Give the extent of all uninfected red blood cells.
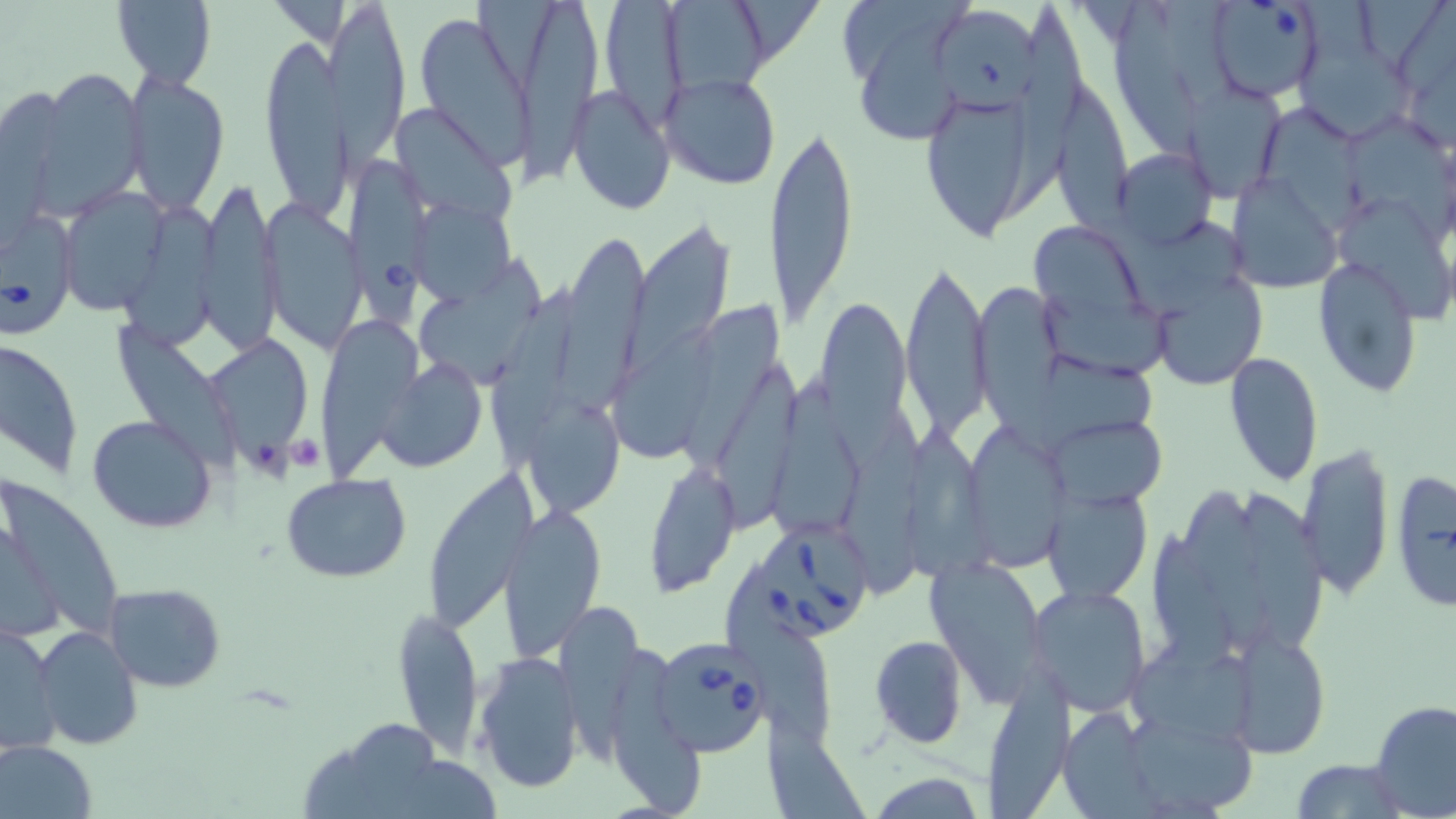

Approximate bounding boxes as named x1/y1/x2/y2 corners in pixels.
Uninfected red blood cells: (x1=334, y1=0, x2=407, y2=170), (x1=110, y1=1, x2=217, y2=87), (x1=268, y1=1, x2=339, y2=46), (x1=598, y1=1, x2=689, y2=132), (x1=671, y1=1, x2=771, y2=98), (x1=1003, y1=1, x2=1077, y2=220), (x1=845, y1=2, x2=973, y2=84), (x1=1111, y1=2, x2=1200, y2=159), (x1=508, y1=3, x2=599, y2=187), (x1=415, y1=13, x2=534, y2=167), (x1=942, y1=14, x2=1042, y2=117), (x1=261, y1=32, x2=345, y2=228), (x1=856, y1=37, x2=973, y2=137), (x1=1298, y1=47, x2=1414, y2=141), (x1=34, y1=65, x2=147, y2=214), (x1=123, y1=68, x2=230, y2=213), (x1=660, y1=73, x2=782, y2=191), (x1=570, y1=83, x2=676, y2=218), (x1=1181, y1=85, x2=1285, y2=200), (x1=919, y1=87, x2=1047, y2=242), (x1=1055, y1=88, x2=1135, y2=235), (x1=395, y1=111, x2=515, y2=222), (x1=1262, y1=111, x2=1365, y2=241), (x1=1346, y1=117, x2=1456, y2=252), (x1=765, y1=122, x2=860, y2=331), (x1=1114, y1=147, x2=1217, y2=253), (x1=1227, y1=172, x2=1344, y2=292), (x1=197, y1=179, x2=280, y2=354), (x1=59, y1=187, x2=172, y2=315), (x1=263, y1=201, x2=364, y2=354), (x1=418, y1=202, x2=512, y2=304), (x1=126, y1=207, x2=229, y2=361), (x1=1342, y1=209, x2=1454, y2=325), (x1=1029, y1=218, x2=1150, y2=325), (x1=1115, y1=221, x2=1244, y2=320), (x1=631, y1=224, x2=733, y2=352), (x1=556, y1=236, x2=647, y2=417), (x1=901, y1=254, x2=994, y2=443), (x1=1314, y1=256, x2=1425, y2=398), (x1=417, y1=258, x2=542, y2=386), (x1=1154, y1=259, x2=1268, y2=390), (x1=493, y1=278, x2=580, y2=476), (x1=972, y1=280, x2=1061, y2=417), (x1=1046, y1=293, x2=1168, y2=381), (x1=813, y1=296, x2=914, y2=439), (x1=685, y1=308, x2=784, y2=473), (x1=320, y1=322, x2=423, y2=484), (x1=115, y1=328, x2=243, y2=476), (x1=612, y1=329, x2=728, y2=460), (x1=1, y1=336, x2=83, y2=478), (x1=213, y1=338, x2=305, y2=483), (x1=1224, y1=352, x2=1324, y2=488), (x1=1034, y1=359, x2=1166, y2=449), (x1=379, y1=360, x2=486, y2=471), (x1=713, y1=360, x2=804, y2=529), (x1=768, y1=374, x2=854, y2=554), (x1=530, y1=406, x2=617, y2=518), (x1=87, y1=413, x2=218, y2=532), (x1=1057, y1=414, x2=1167, y2=510), (x1=846, y1=421, x2=924, y2=596), (x1=966, y1=422, x2=1073, y2=572), (x1=905, y1=423, x2=987, y2=580), (x1=1298, y1=439, x2=1396, y2=603), (x1=644, y1=458, x2=738, y2=596), (x1=422, y1=467, x2=536, y2=633), (x1=1390, y1=469, x2=1456, y2=615), (x1=282, y1=473, x2=413, y2=584), (x1=2, y1=475, x2=119, y2=639), (x1=1044, y1=486, x2=1152, y2=603), (x1=1184, y1=488, x2=1277, y2=661), (x1=1240, y1=492, x2=1329, y2=651), (x1=498, y1=504, x2=606, y2=657), (x1=1, y1=511, x2=62, y2=645), (x1=1150, y1=537, x2=1243, y2=675), (x1=925, y1=558, x2=1046, y2=712), (x1=104, y1=583, x2=228, y2=693), (x1=1029, y1=584, x2=1153, y2=717), (x1=726, y1=599, x2=837, y2=749), (x1=556, y1=602, x2=643, y2=772), (x1=393, y1=608, x2=485, y2=757), (x1=1, y1=618, x2=61, y2=758), (x1=32, y1=624, x2=142, y2=750), (x1=1226, y1=627, x2=1331, y2=758), (x1=869, y1=635, x2=968, y2=748), (x1=1126, y1=641, x2=1268, y2=754), (x1=615, y1=646, x2=708, y2=818), (x1=475, y1=653, x2=586, y2=795), (x1=986, y1=668, x2=1076, y2=819), (x1=1369, y1=700, x2=1456, y2=818), (x1=1060, y1=708, x2=1160, y2=815), (x1=764, y1=713, x2=865, y2=819), (x1=347, y1=721, x2=437, y2=819), (x1=1133, y1=721, x2=1254, y2=818), (x1=1, y1=740, x2=98, y2=819), (x1=1291, y1=758, x2=1410, y2=819), (x1=869, y1=772, x2=986, y2=818).

slide-level diagnosis = Babesia divergens
stain = May-Grünwald-Giemsa
image size = 1456×819 pixels
Babesia divergens-infected red blood cell locations = approximate bounding boxes as named x1/y1/x2/y2 corners in pixels: (x1=1205, y1=1, x2=1326, y2=102), (x1=346, y1=155, x2=427, y2=327), (x1=0, y1=209, x2=79, y2=337), (x1=759, y1=526, x2=868, y2=644), (x1=658, y1=642, x2=765, y2=758)
field of view = one of a larger specimen
preparation = thin blood film
magnification = 1000x
modality = light microscopy
platelet locations = approximate bounding boxes as named x1/y1/x2/y2 corners in pixels: (x1=284, y1=436, x2=327, y2=473)